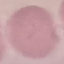

malaria status = uninfected
preparation = thin blood film
stain = Giemsa
capture = smartphone camera at the microscope eyepiece
image type = automatically extracted cell patch, resized to 64 × 64 pixels